State the preparation type.
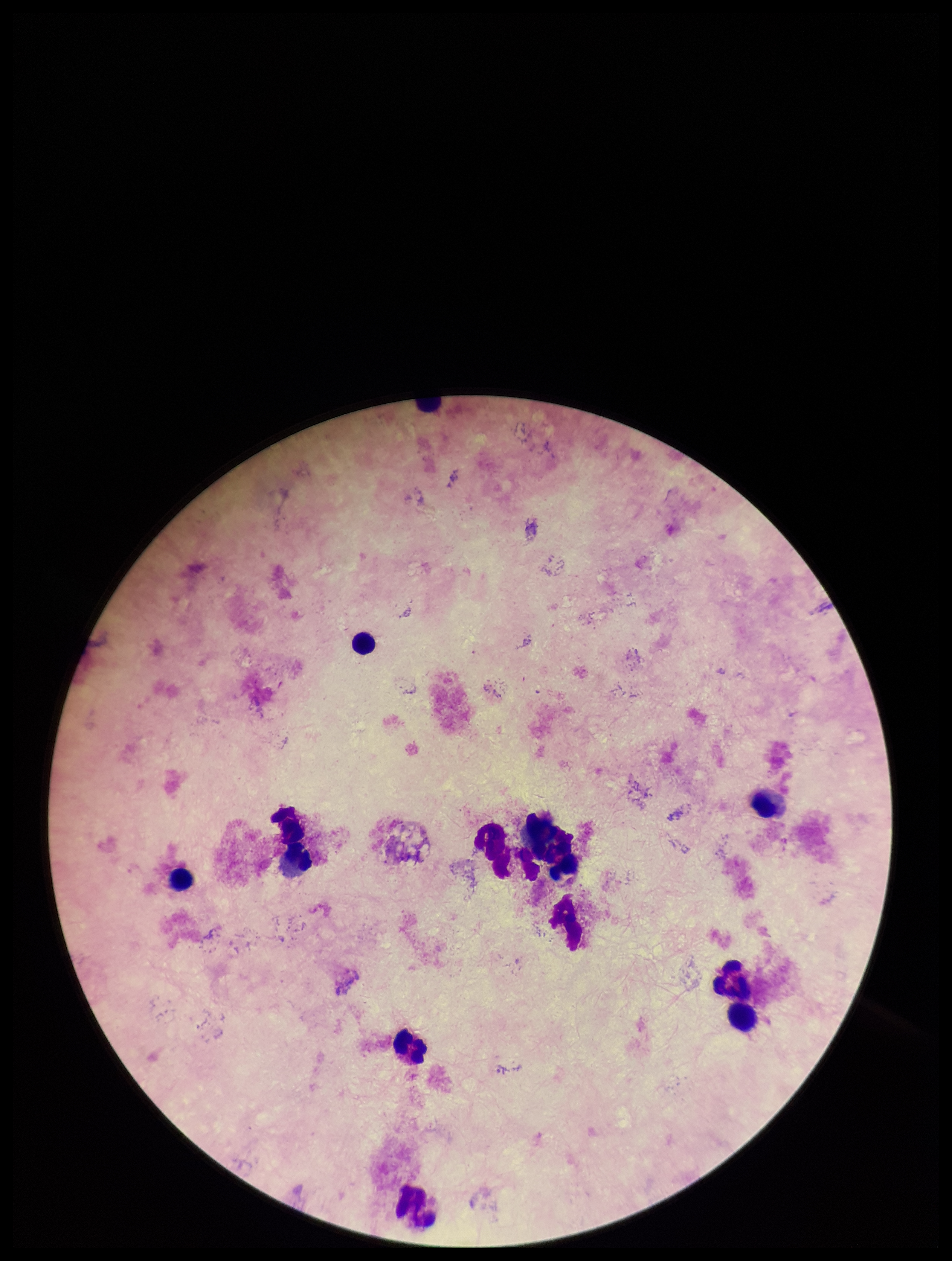
Thick.

Giemsa stain. Plasmodium parasites: none seen. Patient malaria status: negative. Image is 952×1261 pixels. One field from this slide. Photographed through the microscope eyepiece with a smartphone camera. Leukocyte count: 11. Parasite count: 0.